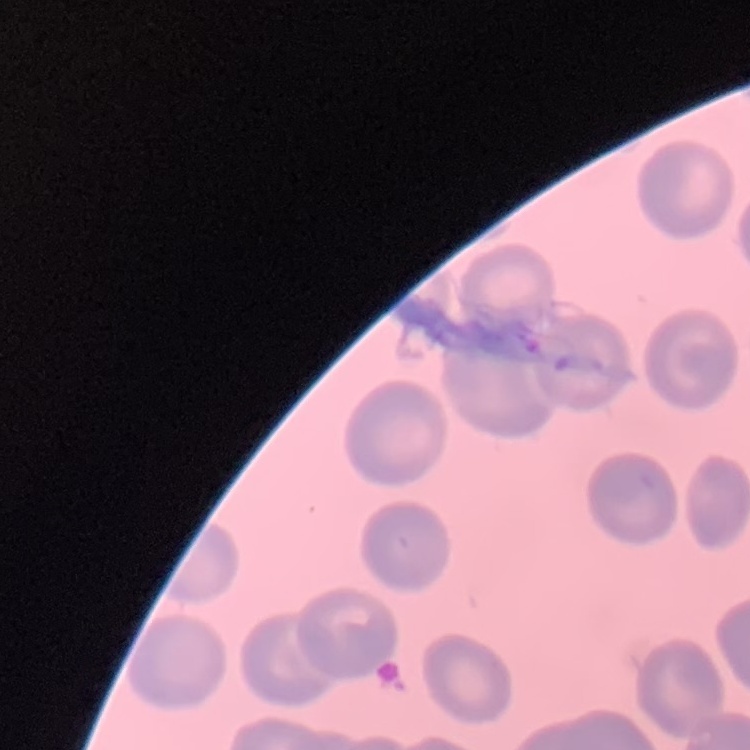
red blood cell morphology = no rouleaux formation
preparation = thin blood film
stain = Field's or Giemsa
image type = one tile cut from a larger photomicrograph